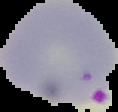

From a thin blood film. Segmented cell region on a black background. Result: malaria parasites identified. Image is 118×112 pixels.